Classify this cell by malaria status.
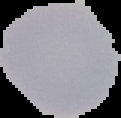

It is uninfected.

Cell region segmented out of the field of view; the surrounding area is masked to black. From a thin blood film. Image is 121×118 pixels.